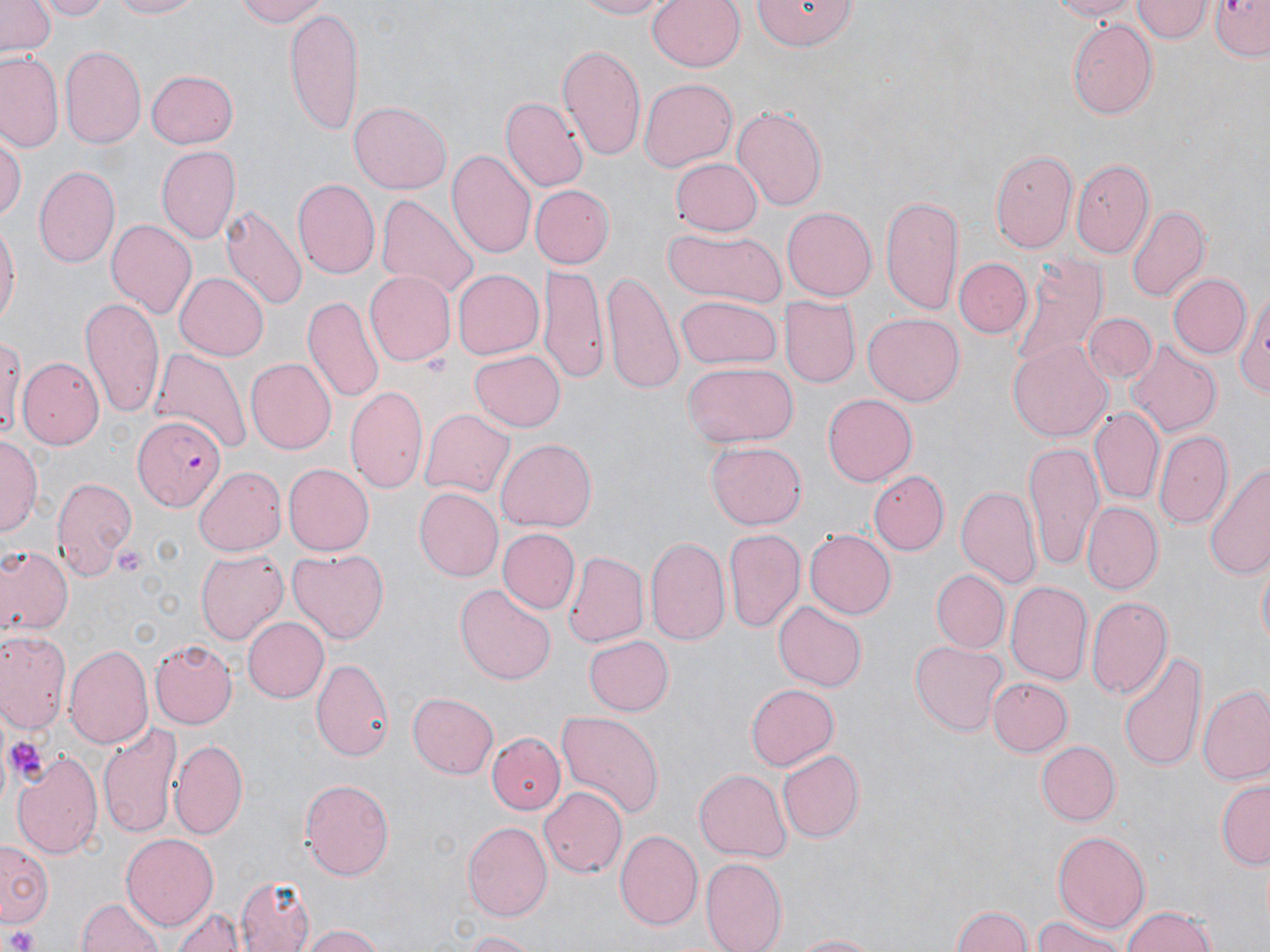
{
  "slide_level_diagnosis": "Plasmodium falciparum",
  "preparation": "thin blood film",
  "modality": "optical microscopy",
  "stain": "May-Grünwald-Giemsa",
  "uninfected_red_blood_cell_locations": "approximate bounding boxes as (x1,y1)-(x2,y2) corner pairs in pixels: (1,0)-(55,56), (40,0)-(111,20), (103,0)-(205,20), (230,0)-(332,27), (573,0)-(672,19), (645,0)-(745,73), (749,0)-(860,52), (1038,0)-(1143,20), (1134,0)-(1209,43), (1207,0)-(1270,60), (286,4)-(365,138), (1066,19)-(1158,119), (558,45)-(646,162), (60,46)-(146,148), (1,52)-(65,153), (145,69)-(239,148), (639,78)-(738,171), (500,96)-(587,192), (350,100)-(453,193), (732,106)-(828,209), (0,133)-(24,222), (155,146)-(240,245), (993,147)-(1078,250), (446,149)-(535,258), (673,156)-(762,237), (1072,161)-(1156,260), (33,166)-(119,269), (293,178)-(379,279), (532,184)-(614,268), (375,194)-(479,303), (881,194)-(966,318), (221,203)-(306,310), (1126,203)-(1209,303), (783,207)-(877,301), (105,216)-(196,317), (0,220)-(18,331), (661,226)-(787,307), (1006,256)-(1107,373), (954,257)-(1031,337), (539,264)-(610,385), (452,268)-(544,360), (362,269)-(455,366), (602,270)-(683,392), (173,272)-(269,362), (1168,273)-(1251,359), (1237,281)-(1270,403), (301,294)-(384,404), (673,295)-(782,370), (778,296)-(859,389), (79,297)-(165,420), (1083,312)-(1158,384), (863,314)-(964,406), (0,327)-(22,443), (1008,337)-(1112,443), (1124,340)-(1223,437), (150,346)-(250,459), (468,350)-(564,432), (18,354)-(103,448), (246,359)-(336,454), (680,362)-(795,448), (344,385)-(429,496), (822,394)-(916,484), (421,407)-(516,499), (1091,408)-(1165,503), (1154,428)-(1232,528), (1,437)-(39,539), (495,438)-(596,533), (706,441)-(805,529), (1024,442)-(1103,571), (1206,462)-(1270,581), (284,464)-(373,556), (193,467)-(286,555), (870,470)-(949,555), (51,475)-(136,581), (955,484)-(1040,590), (414,487)-(503,580), (1082,501)-(1161,595), (499,528)-(579,614), (724,528)-(804,633), (804,529)-(896,618), (645,536)-(732,645), (0,544)-(71,641), (287,546)-(390,644), (195,548)-(288,645), (565,551)-(648,647), (1254,560)-(1269,649), (933,569)-(1009,652), (1006,580)-(1092,686), (455,582)-(554,682), (1088,595)-(1172,700), (772,601)-(866,691), (243,616)-(331,703), (0,631)-(70,735), (581,635)-(674,716), (150,639)-(236,728), (910,639)-(1008,736), (65,644)-(152,749), (1121,649)-(1207,771), (312,656)-(393,760), (988,679)-(1073,756), (744,683)-(840,772), (1198,683)-(1270,787), (407,692)-(499,778), (555,708)-(665,817), (97,721)-(181,838), (486,732)-(565,814), (169,736)-(247,838), (1035,739)-(1119,826), (774,748)-(866,845), (11,749)-(103,862), (694,768)-(790,861), (297,779)-(397,881), (1216,781)-(1269,868), (538,787)-(626,878), (463,820)-(551,917), (1052,829)-(1150,933), (614,831)-(702,932), (121,834)-(217,932), (1,842)-(50,926), (700,858)-(787,952), (235,876)-(317,952), (77,896)-(165,952), (171,905)-(244,952), (948,905)-(1035,952), (1120,905)-(1218,952), (1031,917)-(1127,952), (303,925)-(386,952), (457,930)-(543,952), (784,932)-(889,951)",
  "image_size": "1270×952 pixels",
  "field_of_view": "single",
  "platelet_locations": "approximate bounding boxes as (x1,y1)-(x2,y2) corner pairs in pixels: (115,543)-(147,574), (9,738)-(44,778), (4,926)-(40,952)",
  "magnification": "1000x",
  "plasmodium_falciparum_infected_red_blood_cell_locations": "approximate bounding boxes as (x1,y1)-(x2,y2) corner pairs in pixels: (133,414)-(225,512)"
}